Classify this cell by malaria status.
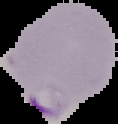
Parasitized.

Summary:
  - Preparation: thin blood film
  - Image size: 118×124 pixels
  - Image type: segmented cell region with the area outside set to black